Assess this cell for malaria.
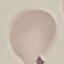
It is uninfected.

Summary:
  - Preparation: thin blood film
  - Image type: automatically extracted cell patch, resized to 64 × 64 pixels
  - Stain: Giemsa
  - Capture: smartphone camera at the microscope eyepiece